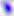
Captured at 400x magnification. Toxoplasma gondii is shown. Photomicrograph.